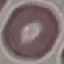

Summary:
  - Malaria status: uninfected
  - Capture: smartphone through the microscope eyepiece
  - Image type: automatically extracted cell patch, resized to 64 × 64 pixels
  - Preparation: thin blood film
  - Stain: Giemsa